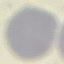

result = no malaria parasites detected
preparation = thin blood film
image type = automatically extracted cell patch, resized to 64 × 64 pixels
capture = smartphone through the microscope eyepiece
stain = Giemsa